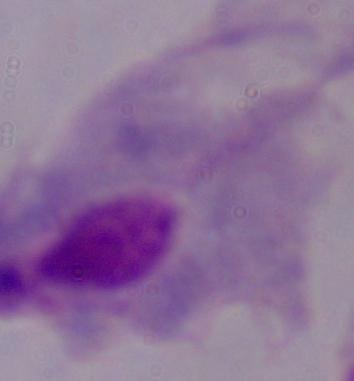
{
  "identification": "trichomonad",
  "magnification": "1000x",
  "modality": "micrograph"
}